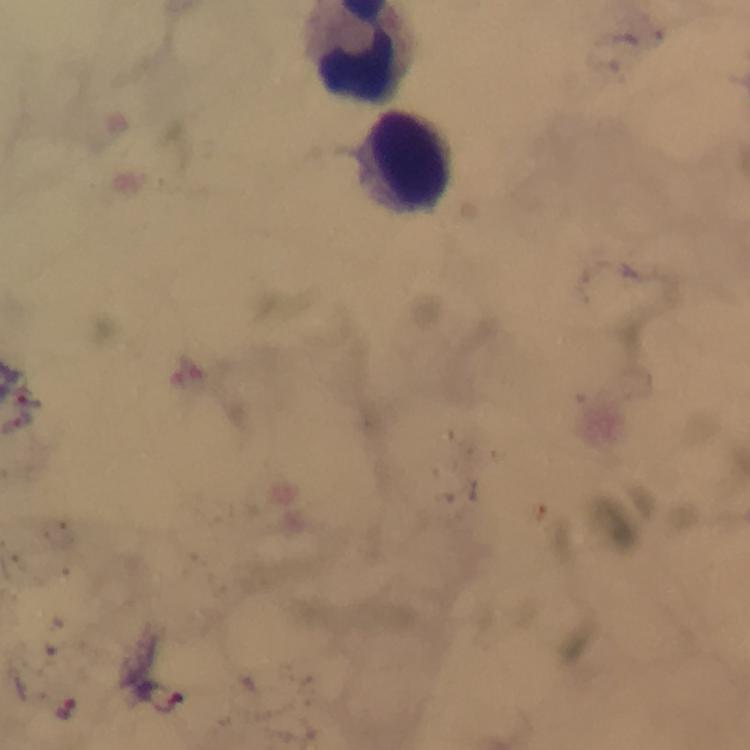
Approximate centers as {x, y} in pixels.
Summary:
  - Leukocyte locations: {405, 153}
  - Plasmodium parasite locations: {30, 397}, {22, 416}, {169, 707}, {65, 708}
  - Image size: 750×750 pixels
  - Context: from a malaria diagnostic workup
  - Stain: Giemsa
  - Capture: smartphone photograph through a microscope
  - Preparation: thick smear
  - Magnification: 100x
  - Cropped from: a single field of view
  - Immersion oil: used